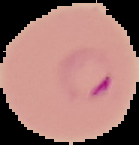
From a thin blood smear. Segmented cell region on a black background. Image is 139×145 pixels. Result: malaria parasites detected.